Report the malaria status of this cell.
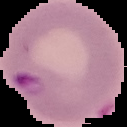
It is parasitized.

Summary:
  - Image type: segmented cell region on a black background
  - Image size: 127×127 pixels
  - Preparation: thin blood smear